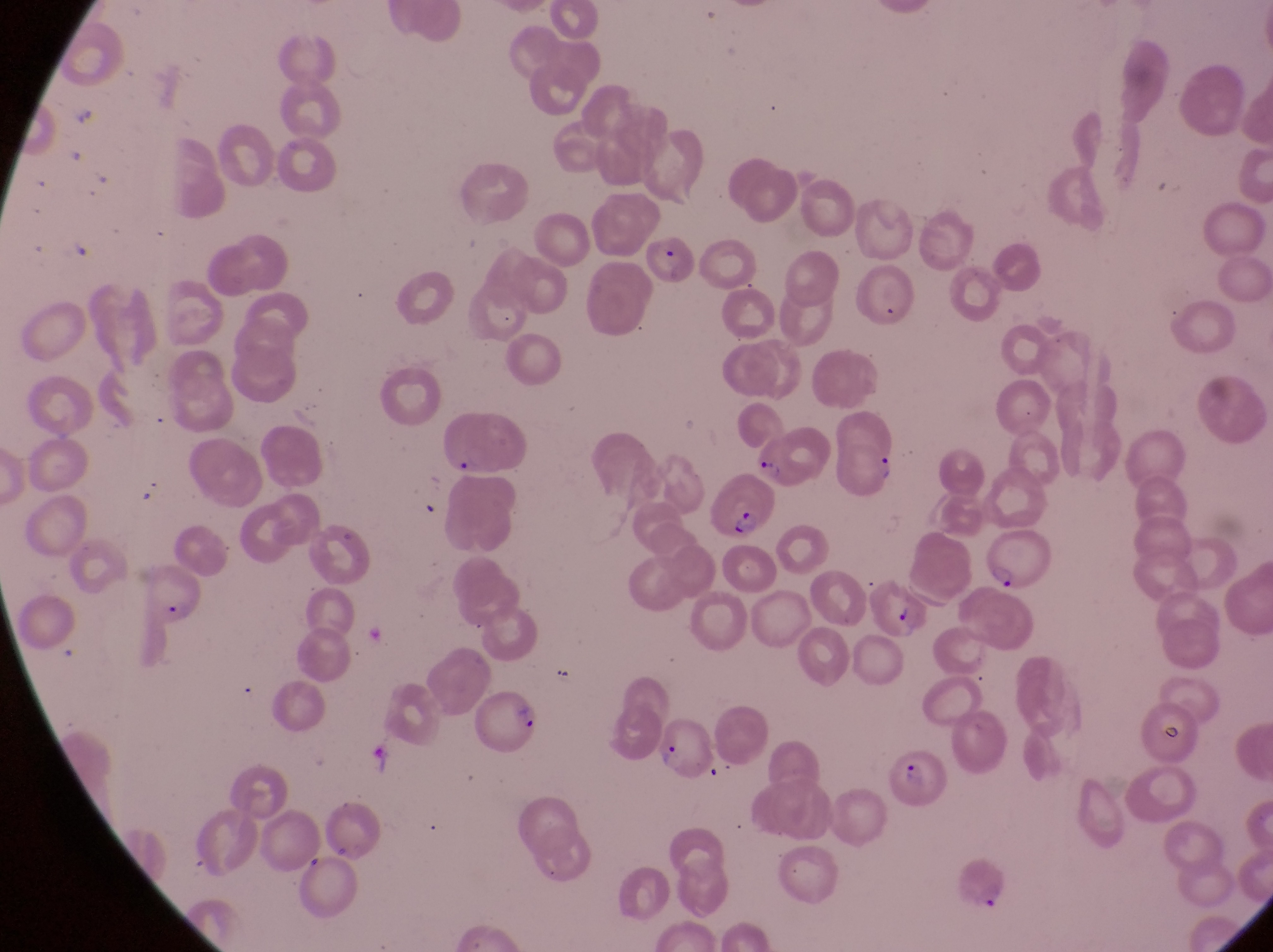

Approximate bounding boxes as (left, top, right, bottom) in pixels. Parasitised red blood cell locations: (833, 414, 899, 499), (702, 472, 774, 539), (986, 534, 1056, 596), (472, 684, 549, 759), (651, 712, 716, 782), (879, 741, 944, 811), (956, 861, 1008, 912). Single field of view. Thin blood film. At a magnification of 1000x. Image is 1273×952 pixels. Collected in Uganda. Captured by a smartphone held over the eyepiece of an Olympus CX-23 microscope.